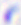

{
  "modality": "micrograph",
  "identification": "Toxoplasma gondii",
  "magnification": "400x"
}